Comment on the morphology of the red blood cells.
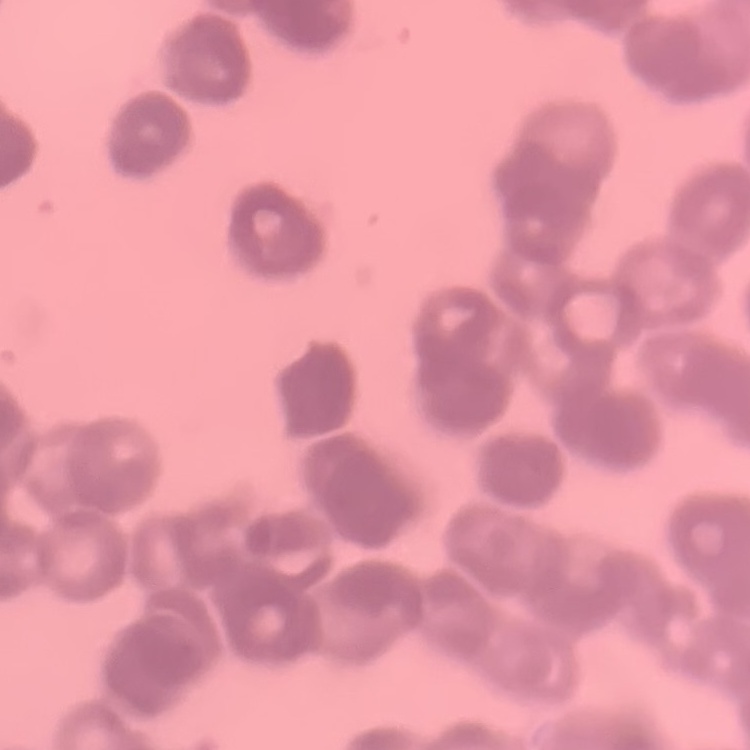
Rouleaux formation.

Thin peripheral smear. One tile cut from a larger photomicrograph. Stained with either Field's or Giemsa.